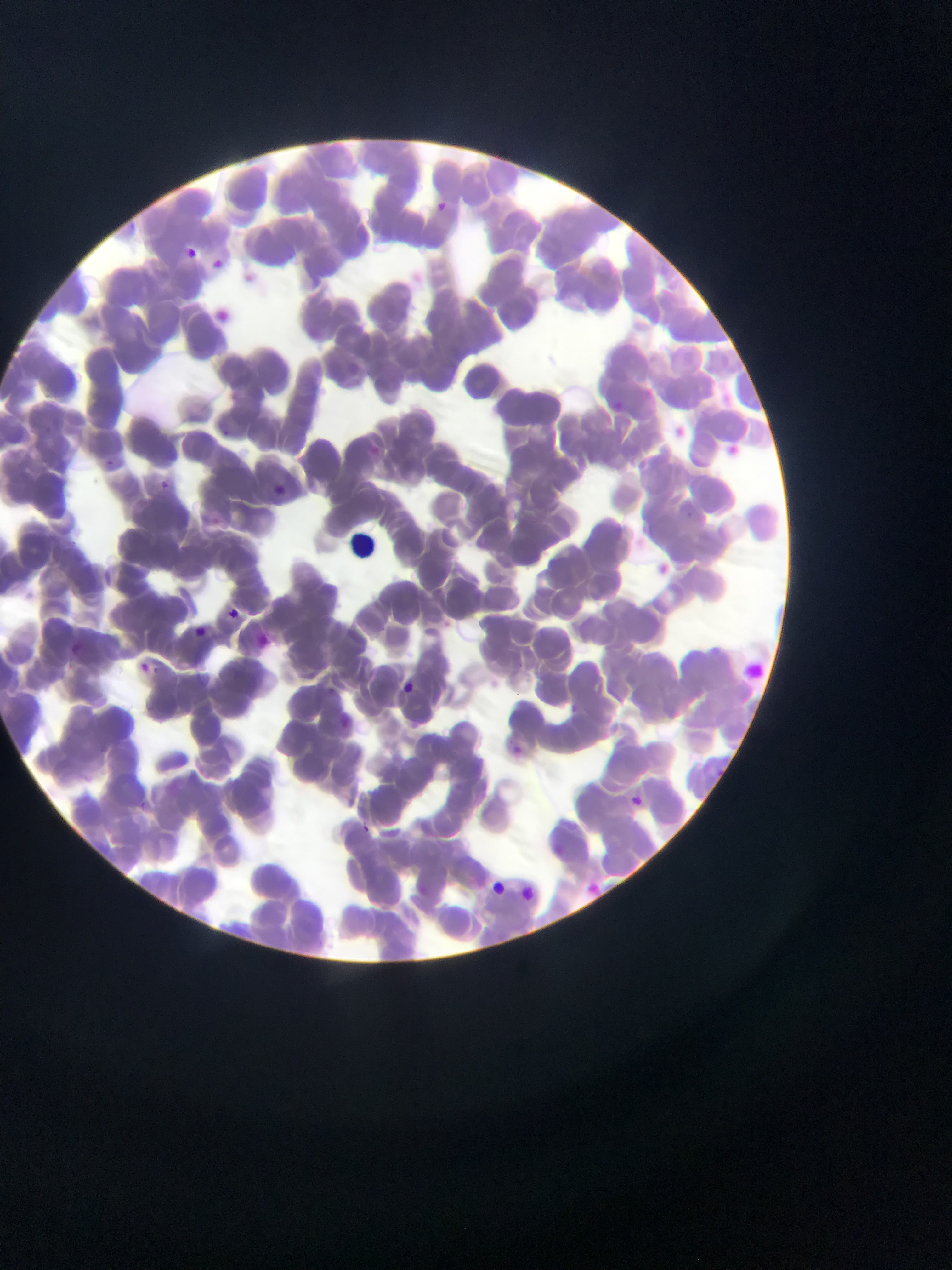

Approximate bounding boxes as (left, top, right, bottom) in pixels.
Summary:
  - Plasmodium parasite locations: (430, 198, 451, 217), (178, 242, 201, 262), (207, 252, 228, 273), (239, 268, 260, 287), (211, 306, 236, 329), (638, 383, 659, 403), (676, 421, 692, 440), (725, 437, 745, 460), (156, 478, 172, 493), (270, 481, 289, 499), (651, 558, 676, 580), (217, 602, 251, 633), (222, 603, 244, 624), (189, 620, 211, 641), (249, 632, 273, 653), (397, 679, 417, 698), (509, 737, 534, 764), (625, 791, 647, 811), (356, 820, 374, 836), (578, 876, 607, 903), (484, 877, 510, 899)
  - Preparation: thin blood smear
  - Image size: 952×1270 pixels
  - Country: Ghana
  - Capture: mobile-phone photograph through a microscope
  - Field of view: single